Assess this cell for malaria.
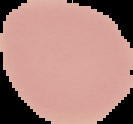

Uninfected.

image size = 133×124 pixels
preparation = thin blood film
image type = segmented cell region with the area outside set to black